Identify the blood parasite species.
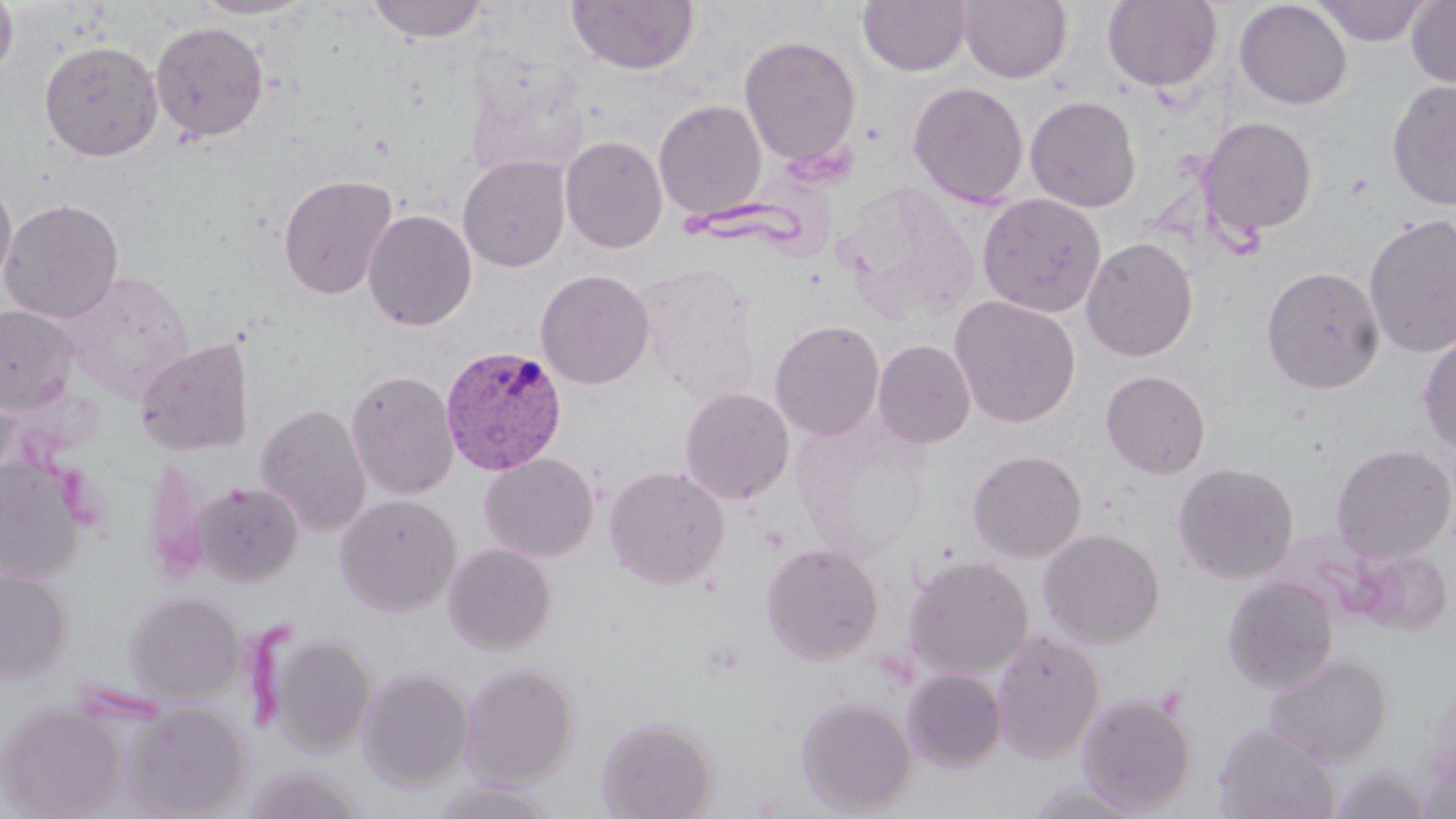
Plasmodium vivax.

Summary:
  - Coordinate format: approximate bounding boxes as [x1, y1, x2, y2] in pixels
  - Uninfected red blood cell locations: [0, 0, 18, 84], [190, 0, 319, 20], [364, 0, 491, 43], [566, 0, 700, 77], [857, 0, 972, 77], [956, 0, 1072, 85], [1406, 0, 1456, 92], [1102, 1, 1223, 95], [1233, 1, 1352, 111], [1313, 1, 1430, 46], [149, 20, 270, 145], [738, 35, 862, 168], [39, 41, 164, 162], [1386, 79, 1456, 210], [907, 81, 1029, 208], [1025, 95, 1142, 213], [653, 99, 767, 221], [1197, 116, 1318, 240], [560, 135, 668, 254], [458, 155, 571, 272], [277, 173, 398, 300], [0, 174, 17, 296], [977, 193, 1107, 318], [1, 199, 124, 324], [362, 208, 477, 332], [1362, 213, 1456, 359], [1081, 236, 1198, 362], [636, 260, 761, 402], [1260, 266, 1385, 395], [535, 269, 655, 390], [948, 295, 1081, 428], [0, 304, 79, 414], [769, 318, 885, 441], [1417, 331, 1456, 455], [134, 337, 255, 456], [873, 339, 976, 448], [345, 368, 460, 501], [1100, 370, 1211, 478], [679, 386, 795, 505], [254, 403, 372, 536], [1331, 444, 1455, 562], [967, 449, 1087, 563], [479, 453, 599, 561], [0, 455, 86, 583], [1172, 462, 1299, 584], [603, 464, 730, 590], [192, 481, 304, 587], [334, 493, 462, 617], [1038, 528, 1165, 648], [442, 542, 557, 655], [759, 542, 884, 665], [1351, 546, 1453, 635], [902, 554, 1033, 681], [0, 566, 72, 682], [1223, 576, 1339, 693], [124, 591, 246, 705], [992, 628, 1105, 763], [267, 631, 377, 758], [1265, 653, 1392, 767], [460, 662, 580, 788], [358, 666, 475, 791], [901, 668, 1008, 772], [1077, 693, 1197, 813], [795, 696, 918, 816], [121, 700, 250, 818], [1, 702, 127, 819], [596, 716, 719, 819], [1215, 722, 1340, 819], [241, 765, 367, 819], [1330, 765, 1431, 818], [429, 779, 559, 819]
  - Plasmodium vivax-infected red blood cell locations: [440, 344, 568, 476]
  - Field of view: one of a larger specimen
  - Stain: May-Grünwald-Giemsa
  - Preparation: thin blood smear
  - Modality: light microscopy
  - Magnification: 1000x
  - Image size: 1456×819 pixels